Assess this cell for malaria.
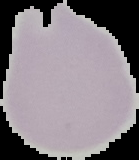
Uninfected.

Summary:
  - Image type: segmented cell region with the area outside set to black
  - Preparation: thin blood film
  - Image size: 139×160 pixels